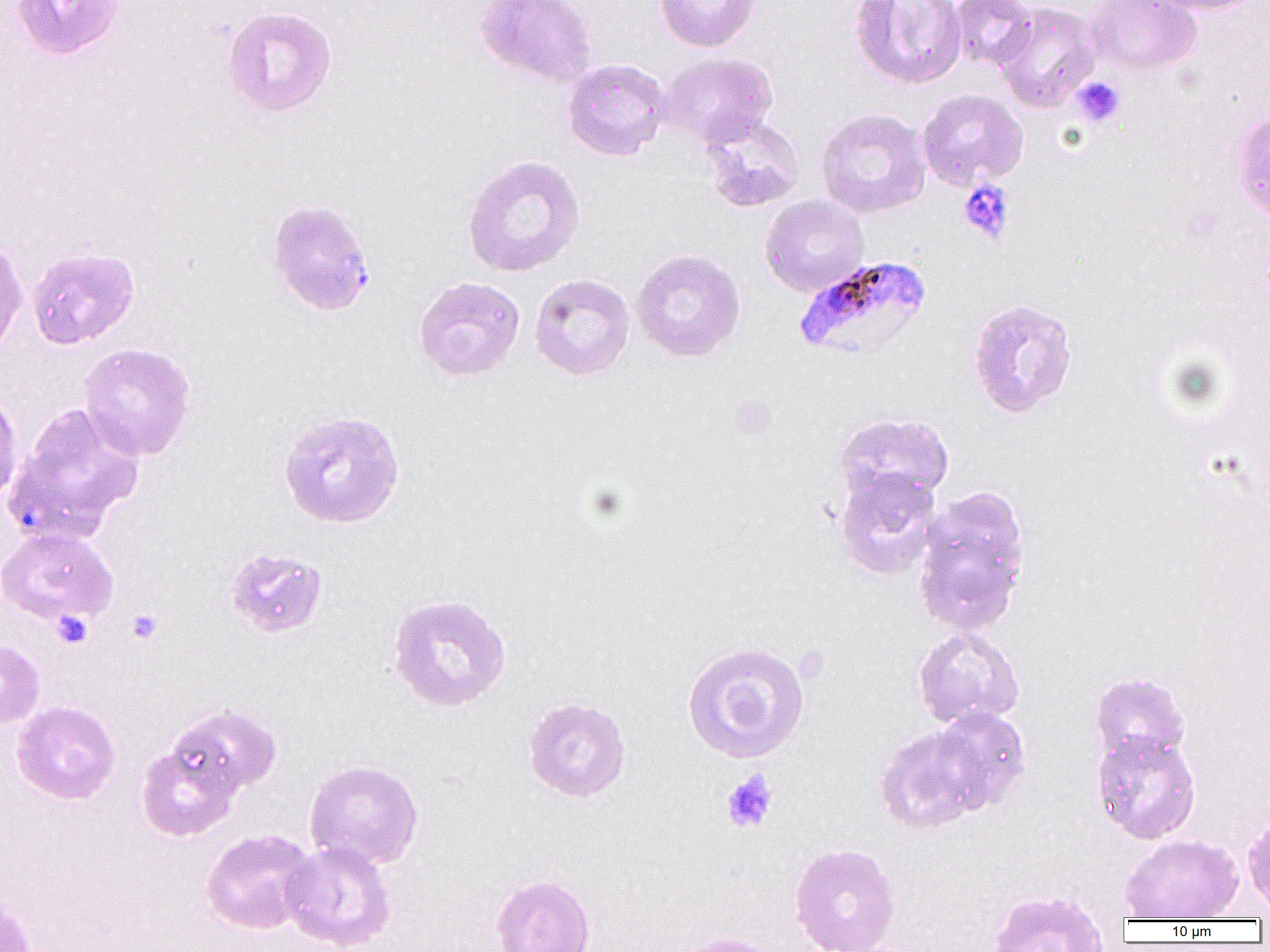

Summary:
  - Coordinate format: approximate bounding boxes as (x1,y1)-(x2,y2) corner pairs in pixels
  - Plasmodium falciparum-infected red blood cell locations: (793,254)-(933,360)
  - Uninfected red blood cell locations: (10,0)-(125,60), (474,0)-(599,89), (653,0)-(761,52), (848,0)-(967,90), (950,0)-(1035,71), (1086,0)-(1202,76), (1145,0)-(1266,15), (994,1)-(1101,112), (220,5)-(337,119), (658,52)-(776,147), (561,57)-(671,161), (916,88)-(1028,191), (815,108)-(931,219), (1233,109)-(1270,223), (699,113)-(806,212), (461,154)-(585,278), (759,194)-(869,297), (264,198)-(376,316), (0,234)-(28,357), (26,246)-(140,350), (630,248)-(746,362), (529,273)-(635,381), (413,276)-(525,383), (965,297)-(1079,419), (77,342)-(197,461), (0,390)-(23,505), (9,402)-(145,539), (277,409)-(405,530), (833,412)-(954,506), (834,468)-(943,579), (913,486)-(1032,635), (0,527)-(119,627), (223,547)-(330,639), (386,592)-(512,712), (912,627)-(1025,729), (0,639)-(45,728), (681,639)-(811,764), (1088,671)-(1190,765), (520,695)-(632,804), (12,700)-(121,805), (163,703)-(282,802), (929,706)-(1033,814), (872,725)-(986,834), (1091,730)-(1201,844), (136,738)-(242,843), (303,759)-(424,870), (1241,812)-(1270,915), (200,829)-(317,934), (1119,833)-(1245,921), (280,840)-(397,951), (788,842)-(901,952), (490,873)-(596,952), (986,888)-(1109,951), (0,890)-(37,952), (673,931)-(785,952)
  - Platelet locations: (1071,76)-(1126,127), (958,180)-(1014,243), (729,395)-(777,439), (126,609)-(163,644), (52,610)-(93,648), (720,769)-(779,834)
  - Slide-level diagnosis: Plasmodium falciparum
  - Magnification: 1000x
  - Modality: optical microscopy
  - Field of view: one of a larger specimen
  - Image size: 1270×952 pixels
  - Preparation: thin blood film